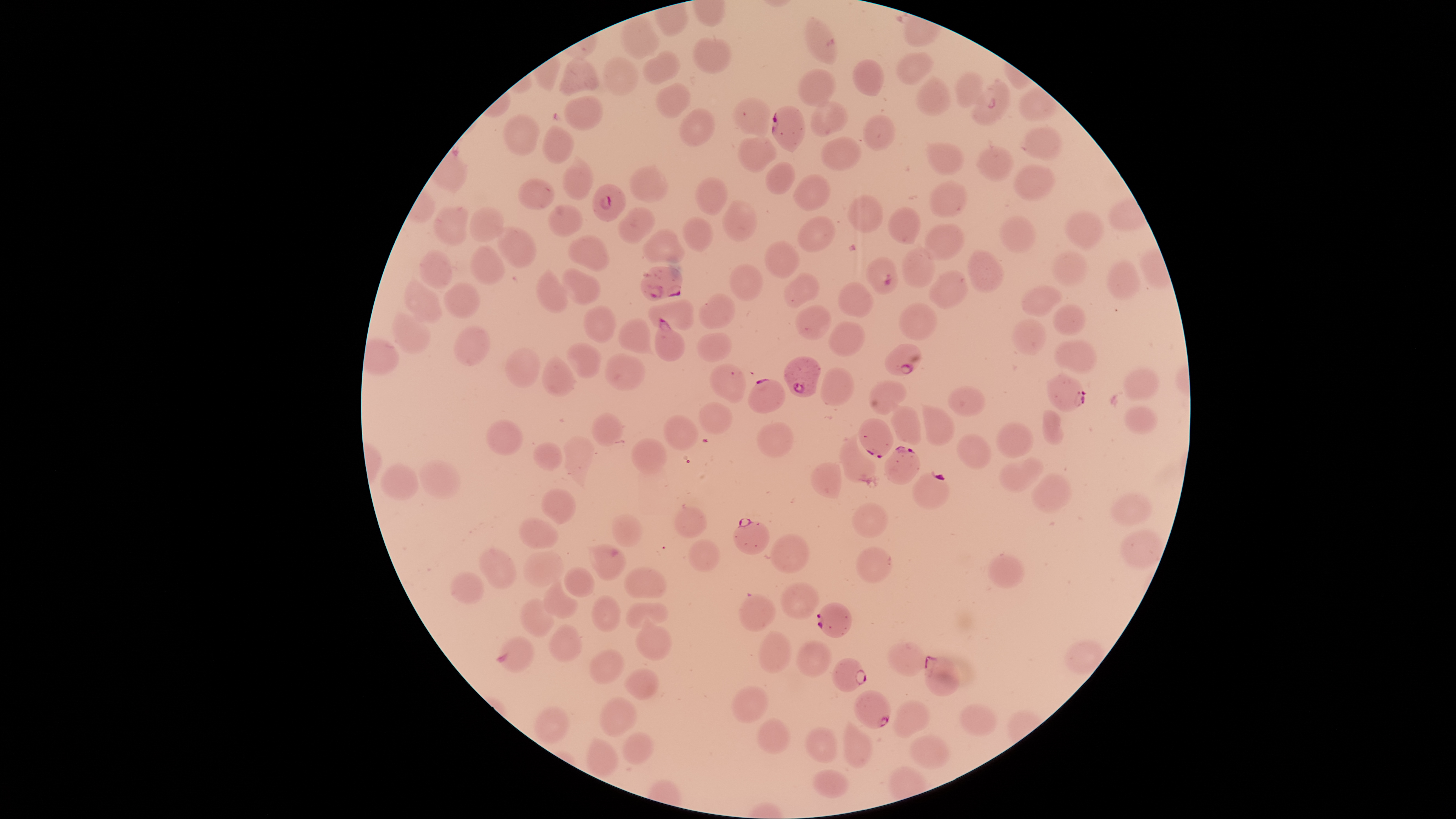
image_size: 1456×819 pixels
species: Plasmodium falciparum
stain: Giemsa
preparation: thin blood film
parasitized_RBCs: 'approximate bounding boxes, in pixels from the top-left corner: (left=970, top=78, right=1011, bottom=126), (left=771, top=105, right=806, bottom=152), (left=591, top=182, right=626, bottom=222), (left=865, top=256, right=898, bottom=295), (left=639, top=265, right=683, bottom=301), (left=653, top=317, right=685, bottom=362), (left=884, top=343, right=922, bottom=377), (left=783, top=355, right=822, bottom=397), (left=1045, top=371, right=1086, bottom=412), (left=747, top=378, right=786, bottom=414), (left=857, top=417, right=894, bottom=458), (left=883, top=445, right=921, bottom=485), (left=912, top=471, right=951, bottom=509), (left=733, top=518, right=771, bottom=555), (left=816, top=602, right=852, bottom=638), (left=495, top=635, right=535, bottom=674), (left=923, top=654, right=961, bottom=696), (left=831, top=657, right=868, bottom=693), (left=853, top=690, right=892, bottom=730)'
presence: malaria parasites identified
field_of_view: single
capture: smartphone photograph through the microscope eyepiece
visible_region: circular
uninfected_RBCs: 'approximate bounding boxes, in pixels from the top-left corner: (left=620, top=14, right=661, bottom=60), (left=805, top=15, right=837, bottom=66), (left=693, top=36, right=733, bottom=74), (left=642, top=50, right=681, bottom=85), (left=896, top=51, right=934, bottom=86), (left=558, top=55, right=599, bottom=95), (left=601, top=56, right=639, bottom=97), (left=851, top=58, right=885, bottom=97), (left=797, top=68, right=836, bottom=108), (left=954, top=71, right=986, bottom=108), (left=915, top=75, right=952, bottom=116), (left=654, top=82, right=691, bottom=119), (left=563, top=94, right=604, bottom=131), (left=731, top=95, right=772, bottom=139), (left=810, top=100, right=848, bottom=138), (left=678, top=107, right=716, bottom=147), (left=502, top=113, right=542, bottom=156), (left=862, top=114, right=897, bottom=151), (left=542, top=124, right=575, bottom=164), (left=1018, top=126, right=1063, bottom=161), (left=736, top=136, right=778, bottom=174), (left=820, top=136, right=863, bottom=171), (left=925, top=141, right=965, bottom=176), (left=975, top=145, right=1014, bottom=182), (left=562, top=153, right=594, bottom=201), (left=765, top=161, right=796, bottom=194), (left=628, top=163, right=670, bottom=203), (left=1013, top=164, right=1055, bottom=201), (left=792, top=173, right=831, bottom=211), (left=695, top=175, right=729, bottom=216), (left=517, top=177, right=556, bottom=210), (left=929, top=180, right=968, bottom=217), (left=847, top=193, right=884, bottom=233), (left=721, top=198, right=757, bottom=242), (left=547, top=203, right=584, bottom=238), (left=432, top=204, right=469, bottom=246), (left=469, top=206, right=505, bottom=243), (left=617, top=206, right=656, bottom=246), (left=886, top=206, right=923, bottom=245), (left=1063, top=210, right=1106, bottom=249), (left=797, top=215, right=836, bottom=252), (left=999, top=215, right=1036, bottom=254), (left=682, top=216, right=714, bottom=253), (left=495, top=223, right=538, bottom=269), (left=923, top=223, right=965, bottom=261), (left=642, top=227, right=685, bottom=264), (left=568, top=234, right=610, bottom=272), (left=763, top=240, right=800, bottom=279), (left=469, top=244, right=506, bottom=286), (left=901, top=246, right=935, bottom=289), (left=966, top=248, right=1005, bottom=294), (left=418, top=249, right=454, bottom=289), (left=1050, top=249, right=1089, bottom=287), (left=1106, top=259, right=1141, bottom=300), (left=729, top=262, right=764, bottom=302), (left=535, top=266, right=569, bottom=314), (left=560, top=267, right=601, bottom=306), (left=927, top=268, right=969, bottom=310), (left=783, top=271, right=821, bottom=309), (left=404, top=275, right=444, bottom=324), (left=444, top=281, right=481, bottom=318), (left=837, top=282, right=874, bottom=318), (left=1021, top=285, right=1065, bottom=317), (left=698, top=292, right=735, bottom=329), (left=647, top=298, right=695, bottom=331), (left=898, top=302, right=938, bottom=341), (left=1051, top=303, right=1087, bottom=336), (left=794, top=304, right=832, bottom=340), (left=583, top=305, right=617, bottom=343), (left=391, top=311, right=431, bottom=355), (left=617, top=317, right=655, bottom=356), (left=1010, top=317, right=1048, bottom=356), (left=828, top=321, right=865, bottom=357), (left=454, top=324, right=491, bottom=366), (left=696, top=332, right=732, bottom=362), (left=1054, top=339, right=1098, bottom=373), (left=565, top=342, right=604, bottom=379), (left=505, top=346, right=541, bottom=388), (left=604, top=352, right=646, bottom=391), (left=541, top=354, right=578, bottom=398), (left=709, top=362, right=747, bottom=404), (left=820, top=367, right=855, bottom=407), (left=1122, top=368, right=1160, bottom=402), (left=867, top=379, right=907, bottom=415), (left=947, top=385, right=986, bottom=418), (left=891, top=400, right=921, bottom=446), (left=698, top=402, right=733, bottom=435), (left=921, top=402, right=956, bottom=447), (left=1123, top=405, right=1158, bottom=435), (left=1041, top=409, right=1064, bottom=446), (left=590, top=412, right=624, bottom=447), (left=662, top=413, right=699, bottom=451), (left=485, top=419, right=523, bottom=455), (left=755, top=421, right=794, bottom=459), (left=995, top=421, right=1035, bottom=457), (left=839, top=434, right=876, bottom=484), (left=956, top=434, right=992, bottom=470), (left=563, top=436, right=595, bottom=490), (left=631, top=437, right=668, bottom=474), (left=533, top=441, right=563, bottom=471), (left=999, top=456, right=1045, bottom=493), (left=417, top=459, right=461, bottom=499), (left=380, top=462, right=421, bottom=502), (left=809, top=462, right=842, bottom=500), (left=1031, top=472, right=1073, bottom=515), (left=540, top=487, right=576, bottom=525), (left=1109, top=492, right=1154, bottom=527), (left=851, top=502, right=889, bottom=538), (left=673, top=505, right=708, bottom=539), (left=611, top=513, right=643, bottom=547), (left=517, top=517, right=560, bottom=549), (left=1120, top=527, right=1164, bottom=570), (left=769, top=532, right=810, bottom=574), (left=687, top=538, right=721, bottom=573), (left=587, top=543, right=627, bottom=581), (left=855, top=546, right=893, bottom=584), (left=478, top=547, right=517, bottom=589), (left=523, top=551, right=565, bottom=586), (left=987, top=553, right=1025, bottom=590), (left=564, top=566, right=596, bottom=598), (left=623, top=566, right=667, bottom=599), (left=449, top=571, right=485, bottom=605), (left=543, top=578, right=578, bottom=619), (left=780, top=581, right=820, bottom=620), (left=738, top=593, right=776, bottom=632), (left=591, top=594, right=621, bottom=632), (left=519, top=598, right=555, bottom=638), (left=624, top=601, right=668, bottom=629), (left=635, top=614, right=672, bottom=661), (left=548, top=623, right=582, bottom=662), (left=757, top=631, right=792, bottom=674), (left=795, top=640, right=832, bottom=677), (left=887, top=642, right=926, bottom=676), (left=588, top=649, right=625, bottom=685), (left=624, top=666, right=660, bottom=702), (left=731, top=686, right=769, bottom=724), (left=597, top=696, right=638, bottom=736), (left=891, top=699, right=930, bottom=738), (left=959, top=703, right=998, bottom=737), (left=533, top=706, right=571, bottom=746), (left=756, top=717, right=791, bottom=755), (left=842, top=720, right=873, bottom=768), (left=804, top=727, right=838, bottom=764), (left=621, top=731, right=655, bottom=765), (left=907, top=734, right=950, bottom=769), (left=585, top=737, right=620, bottom=779), (left=812, top=769, right=850, bottom=798)'